Report the malaria status of this cell.
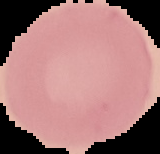

Uninfected.

{
  "image_size": "160×154 pixels",
  "image_type": "cell region segmented out of the field of view; surrounding area masked to black",
  "preparation": "thin blood film"
}